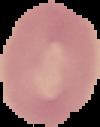

Image is 100×127 pixels. Result: no Plasmodium parasites seen. From a thin blood film. Segmented cell region on a black background.